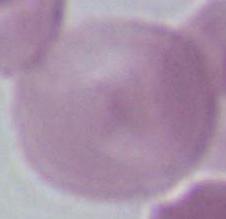

1000x magnification. A red blood cell is seen. Micrograph.